Report the malaria status of this cell.
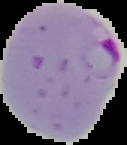

Parasitized.

preparation = thin blood smear
image size = 127×145 pixels
image type = segmented cell region on a black background